Identify the parasite.
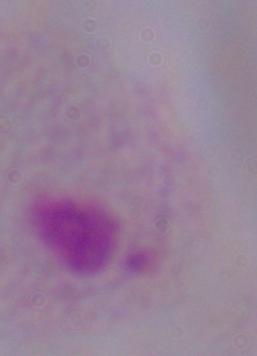
A trichomonad.

1000x magnification. Micrograph.